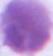
Summary:
  - Identification: erythrocyte
  - Magnification: 1000x
  - Modality: photomicrograph